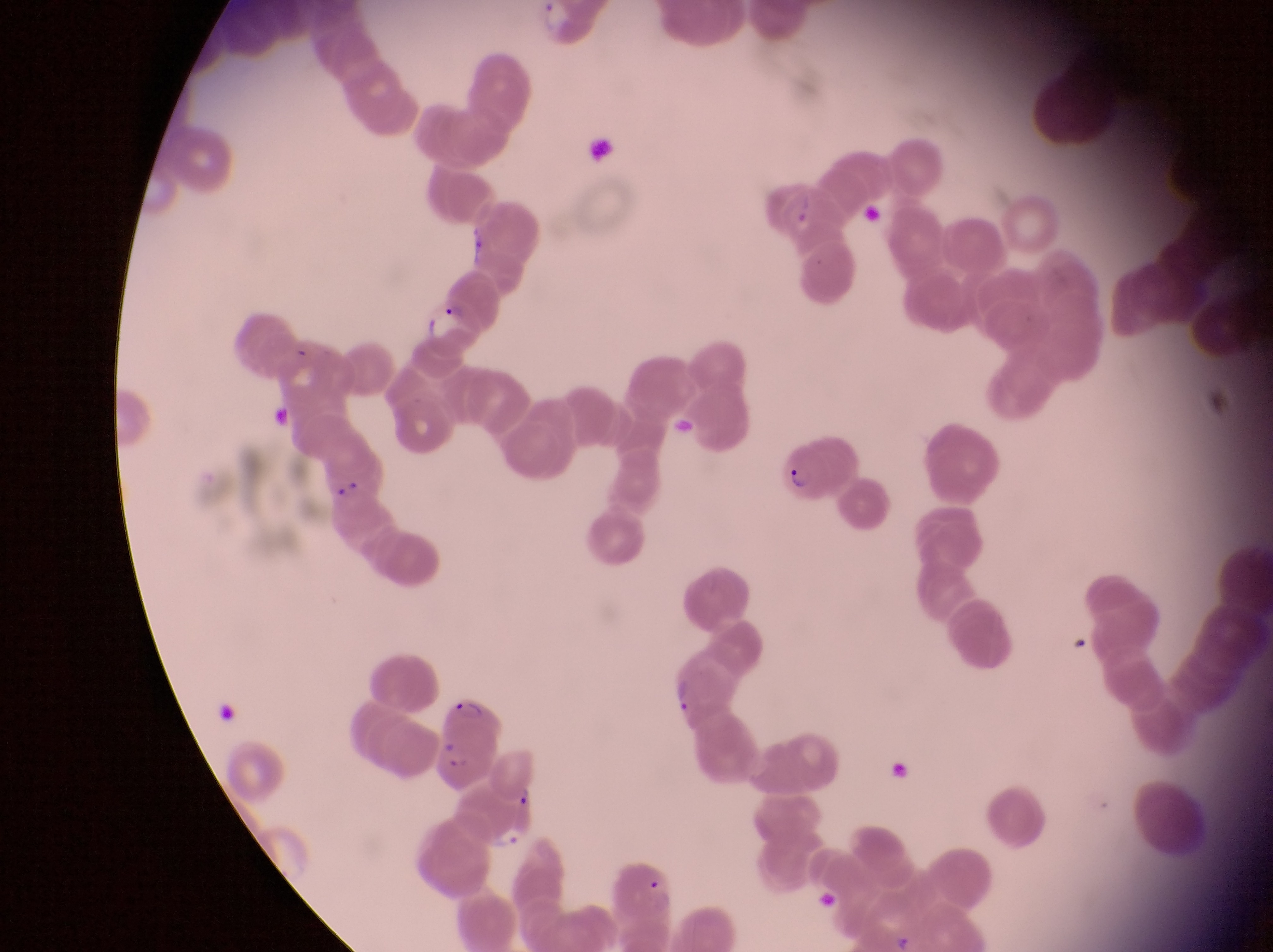

Approximate bounding boxes as (left, top, right, bottom) in pixels.
Summary:
  - Artifact (platelet-like body, stain precipitate, or debris) locations: (588, 134, 622, 180)
  - Parasitised red blood cell locations: (416, 299, 492, 368), (781, 429, 859, 497), (437, 692, 502, 744), (432, 737, 497, 790), (488, 750, 541, 807)
  - Preparation: thin blood film
  - Capture: smartphone photograph through the eyepiece of an Olympus CX-23 microscope
  - Magnification: 1000x
  - Image size: 1273×952 pixels
  - Country: Uganda
  - Field of view: single